Assess this cell for malaria.
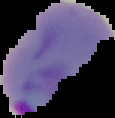

Parasitized.

Image is 115×118 pixels. From a thin blood film. Cell region segmented out of the field of view; the surrounding area is masked to black.